Give the extent of all uninfected red blood cells.
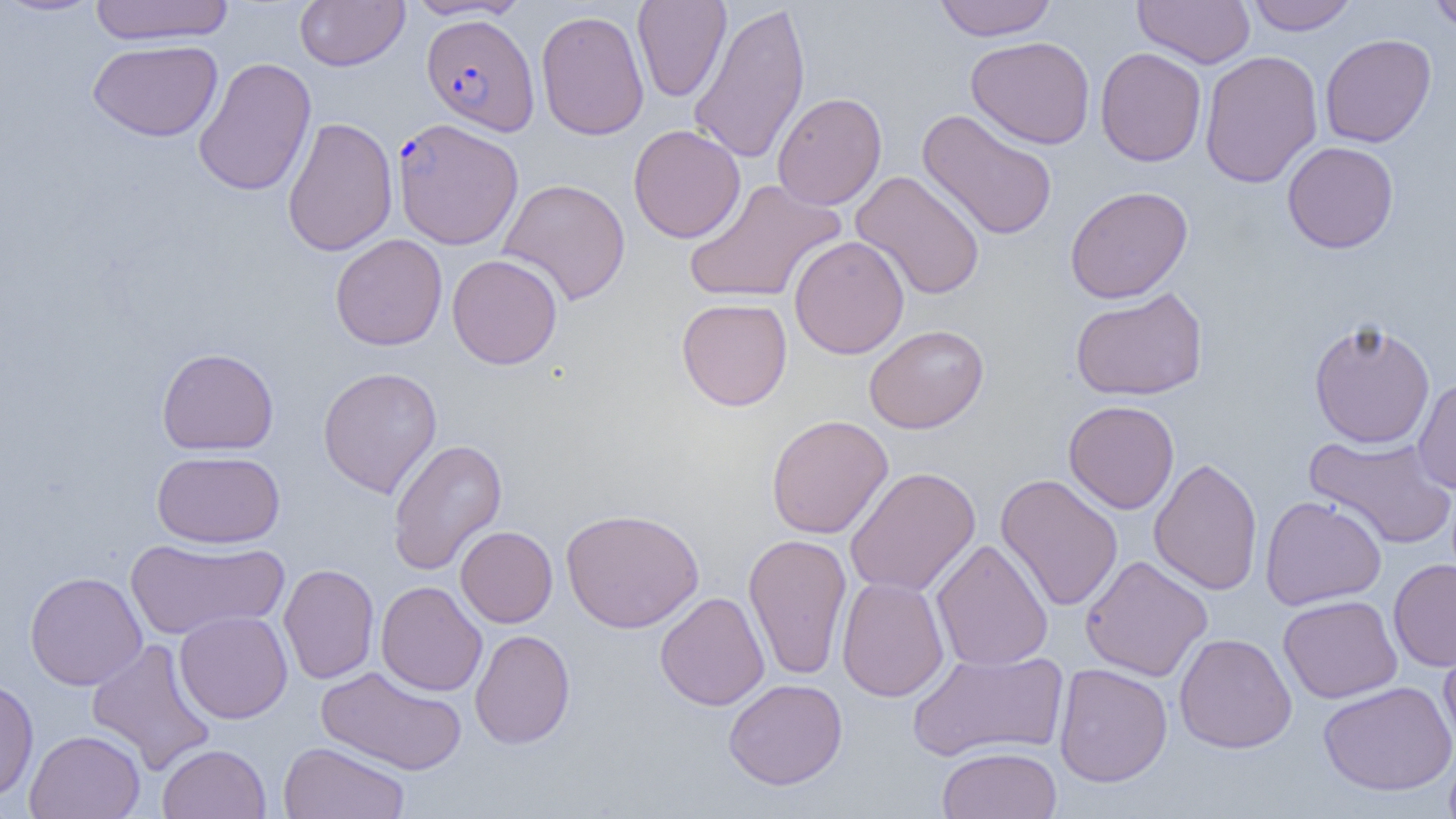
Approximate bounding boxes as named x1/y1/x2/y2 corners in pixels.
Uninfected red blood cells: (x1=0, y1=0, x2=106, y2=18), (x1=89, y1=0, x2=234, y2=46), (x1=295, y1=0, x2=409, y2=71), (x1=402, y1=0, x2=529, y2=21), (x1=632, y1=0, x2=731, y2=102), (x1=933, y1=0, x2=1058, y2=41), (x1=1133, y1=0, x2=1255, y2=68), (x1=1245, y1=0, x2=1359, y2=35), (x1=1426, y1=0, x2=1456, y2=35), (x1=687, y1=2, x2=812, y2=166), (x1=535, y1=10, x2=649, y2=140), (x1=1320, y1=33, x2=1436, y2=148), (x1=966, y1=36, x2=1096, y2=149), (x1=87, y1=39, x2=223, y2=142), (x1=1095, y1=47, x2=1206, y2=167), (x1=1199, y1=50, x2=1323, y2=189), (x1=192, y1=57, x2=317, y2=197), (x1=772, y1=92, x2=887, y2=210), (x1=917, y1=109, x2=1058, y2=241), (x1=282, y1=116, x2=398, y2=256), (x1=628, y1=124, x2=746, y2=243), (x1=1282, y1=141, x2=1399, y2=253), (x1=850, y1=171, x2=986, y2=300), (x1=498, y1=177, x2=631, y2=306), (x1=683, y1=178, x2=846, y2=305), (x1=1065, y1=185, x2=1193, y2=304), (x1=331, y1=234, x2=448, y2=351), (x1=789, y1=235, x2=910, y2=359), (x1=447, y1=253, x2=562, y2=370), (x1=1069, y1=287, x2=1208, y2=402), (x1=676, y1=297, x2=792, y2=411), (x1=1308, y1=318, x2=1437, y2=449), (x1=864, y1=324, x2=989, y2=434), (x1=156, y1=347, x2=279, y2=455), (x1=317, y1=367, x2=442, y2=498), (x1=1412, y1=374, x2=1456, y2=496), (x1=1063, y1=400, x2=1179, y2=514), (x1=766, y1=414, x2=893, y2=539), (x1=1304, y1=433, x2=1456, y2=550), (x1=388, y1=438, x2=507, y2=576), (x1=151, y1=450, x2=285, y2=548), (x1=1148, y1=457, x2=1263, y2=596), (x1=844, y1=467, x2=981, y2=597), (x1=995, y1=473, x2=1123, y2=612), (x1=1147, y1=474, x2=1383, y2=599), (x1=1260, y1=495, x2=1387, y2=610), (x1=560, y1=508, x2=704, y2=633), (x1=455, y1=525, x2=557, y2=628), (x1=743, y1=532, x2=852, y2=681), (x1=124, y1=537, x2=288, y2=640), (x1=931, y1=537, x2=1053, y2=672), (x1=1080, y1=555, x2=1213, y2=682), (x1=1388, y1=558, x2=1456, y2=671), (x1=278, y1=563, x2=379, y2=684), (x1=24, y1=571, x2=147, y2=690), (x1=837, y1=576, x2=950, y2=702), (x1=376, y1=580, x2=487, y2=697), (x1=654, y1=592, x2=770, y2=711), (x1=1278, y1=595, x2=1403, y2=703), (x1=174, y1=610, x2=293, y2=724), (x1=470, y1=629, x2=575, y2=750), (x1=1438, y1=630, x2=1456, y2=751), (x1=1174, y1=633, x2=1297, y2=753), (x1=86, y1=638, x2=216, y2=775), (x1=907, y1=649, x2=1070, y2=762), (x1=1054, y1=662, x2=1172, y2=787), (x1=315, y1=665, x2=467, y2=775), (x1=0, y1=676, x2=38, y2=802), (x1=723, y1=678, x2=848, y2=790), (x1=1318, y1=681, x2=1456, y2=796), (x1=24, y1=730, x2=145, y2=819), (x1=277, y1=740, x2=411, y2=819), (x1=157, y1=743, x2=270, y2=819), (x1=1443, y1=745, x2=1456, y2=819), (x1=936, y1=746, x2=1063, y2=819).

slide-level diagnosis = Plasmodium falciparum
image size = 1456×819 pixels
Plasmodium falciparum-infected red blood cell locations = approximate bounding boxes as named x1/y1/x2/y2 corners in pixels: (x1=421, y1=13, x2=540, y2=135), (x1=392, y1=117, x2=523, y2=249)
field of view = single
magnification = 1000x
modality = light microscopy
preparation = thin blood smear